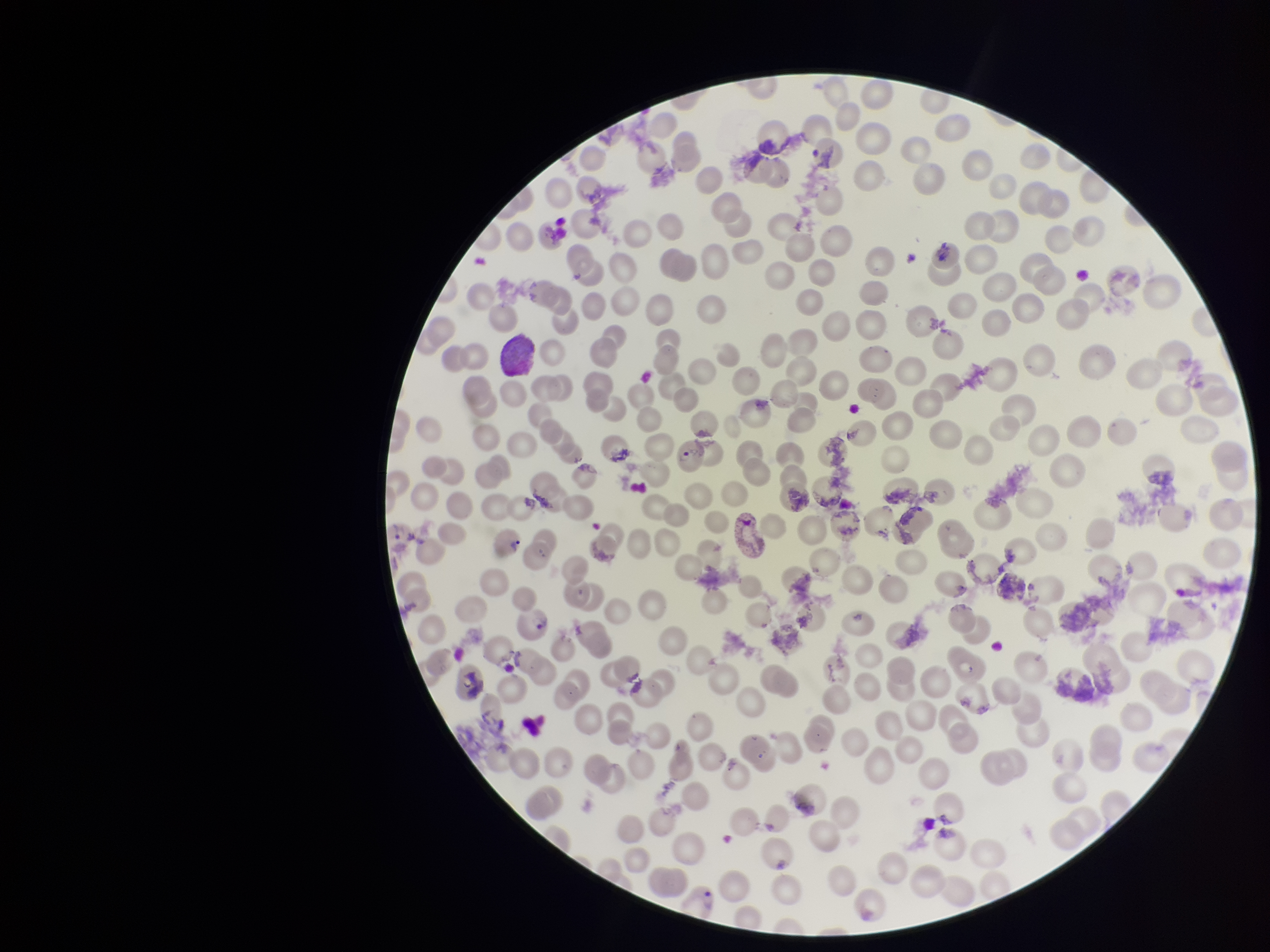

{
  "patient_malaria_status": "positive",
  "image_size": "1270×952 pixels",
  "species_reported_for_this_patient": "Plasmodium vivax",
  "stain": "Giemsa",
  "preparation": "thin",
  "parasitized_red_blood_cells": "seen",
  "capture": "smartphone photograph through the microscope eyepiece",
  "red_blood_cell_count": 231,
  "parasitized_red_blood_cell_count": 4,
  "field_of_view": "single"
}